Classify this cell by malaria status.
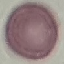

It is uninfected.

image type = automatically extracted cell patch, resized to 64 × 64 pixels
stain = Giemsa
capture = smartphone through the microscope eyepiece
preparation = thin blood film